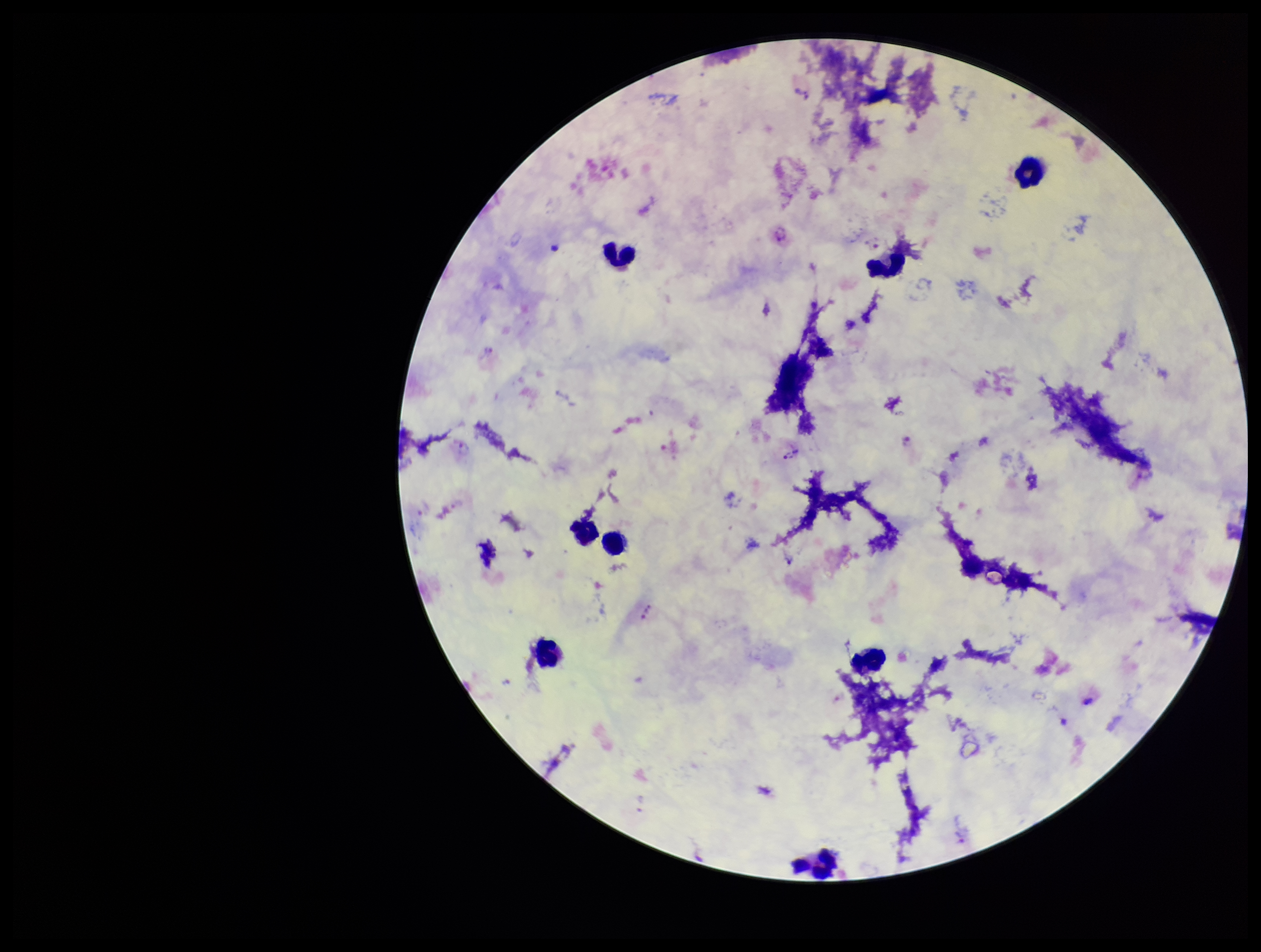

Summary:
  - Leukocyte count: 8
  - Parasite count: 7
  - Plasmodium parasites: detected
  - Stain: Giemsa
  - Patient malaria status: infected
  - Preparation: thick blood smear
  - Species reported for this patient: Plasmodium vivax
  - Capture: smartphone photograph through the microscope eyepiece
  - Field of view: single
  - Image size: 1261×952 pixels